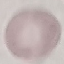
Malaria status: uninfected. Giemsa stain. Automatically extracted cell patch, resized to 64 × 64 pixels. Thin blood film. Photographed with a smartphone camera at the microscope eyepiece.